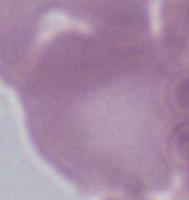

modality = micrograph
magnification = 1000x
identification = erythrocyte